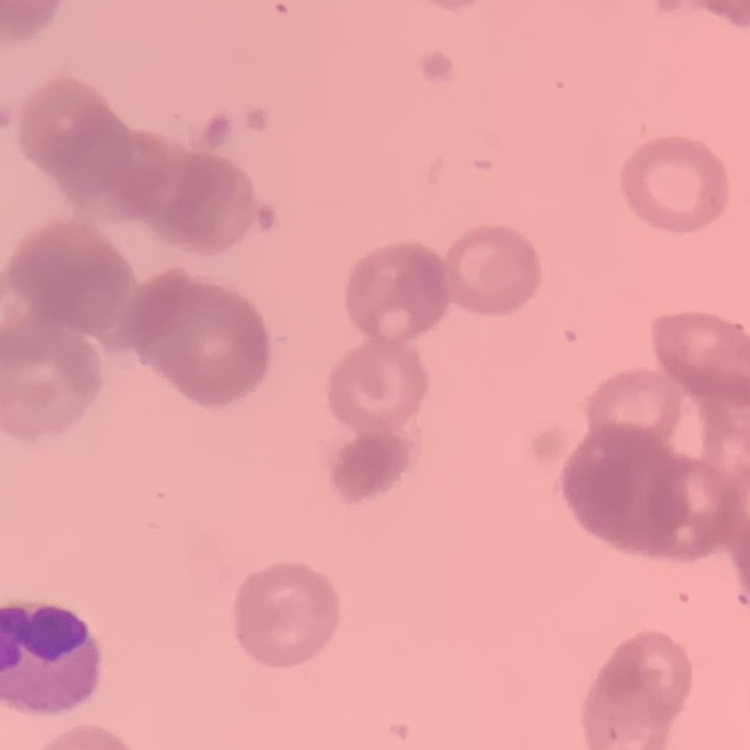

Summary:
  - Erythrocyte morphology: rouleaux formation
  - Image type: one tile cut from a larger photomicrograph
  - Stain: Field's or Giemsa
  - Preparation: thin blood smear